Comment on the morphology of the erythrocytes.
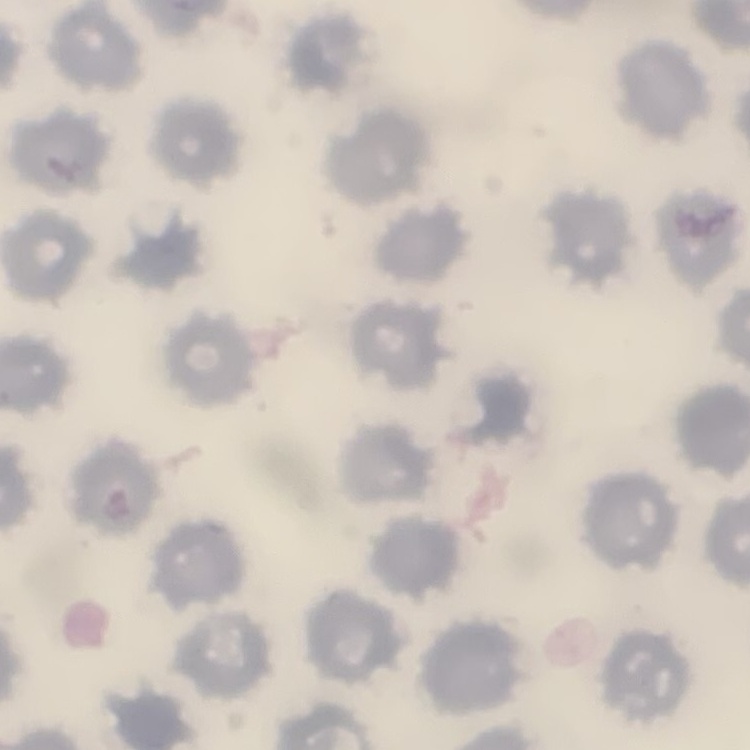

No rouleaux formation.

Summary:
  - Image type: square crop of a larger photomicrograph
  - Preparation: thin blood film
  - Stain: Field's or Giemsa